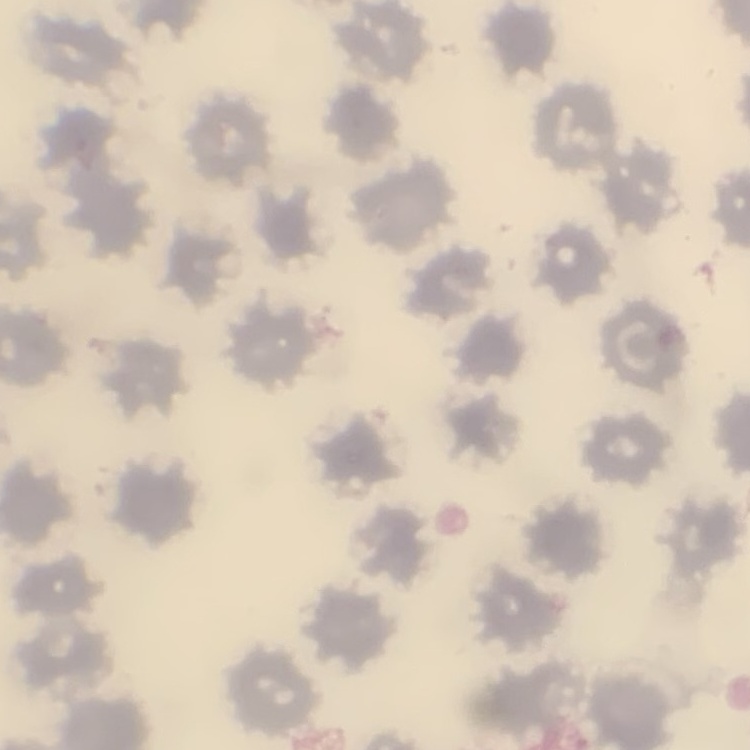
The red blood cells exhibit no rouleaux formation. Thin peripheral smear. Stained with either Field's or Giemsa. Square crop of a larger photomicrograph.